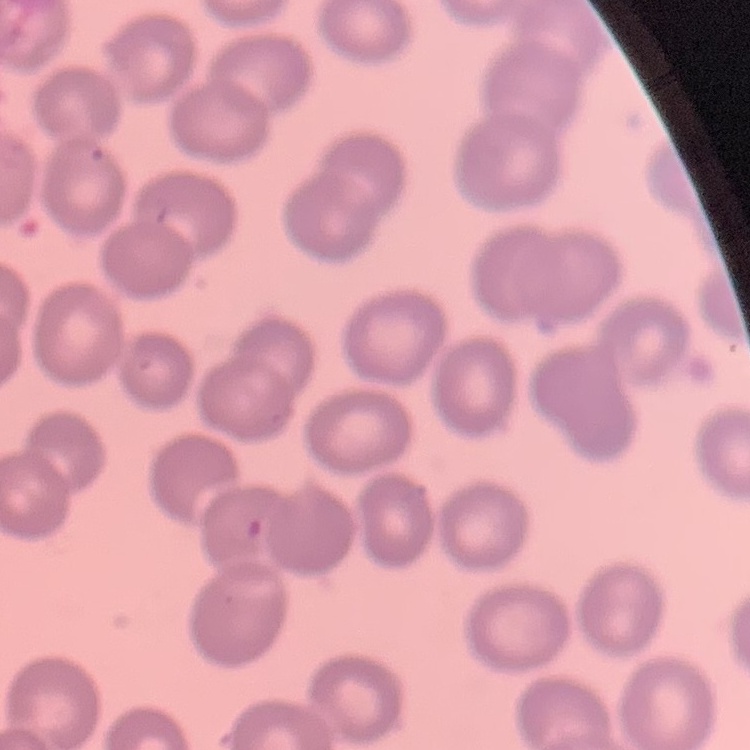

The erythrocytes show no rouleaux formation. One tile cut from a larger photomicrograph. Thin blood film. Field's or Giemsa stain.